Comment on the morphology of the erythrocytes.
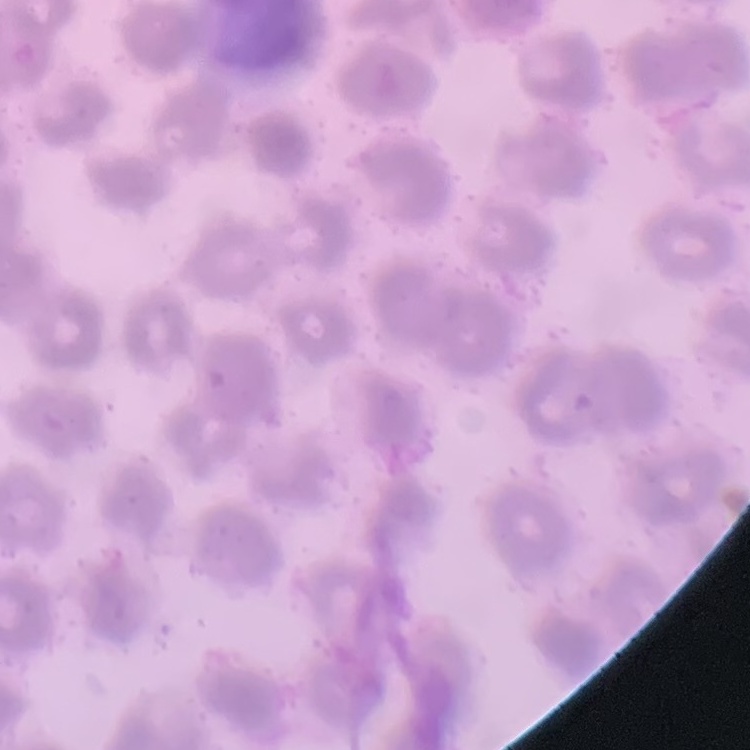
No rouleaux formation.

Square crop of a larger photomicrograph. Field's or Giemsa stain. Thin blood smear.